Classify this cell by malaria status.
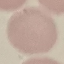
It is uninfected.

stain = Giemsa
capture = smartphone camera at the microscope eyepiece
preparation = thin smear
image type = automatically extracted cell patch, resized to 64 × 64 pixels